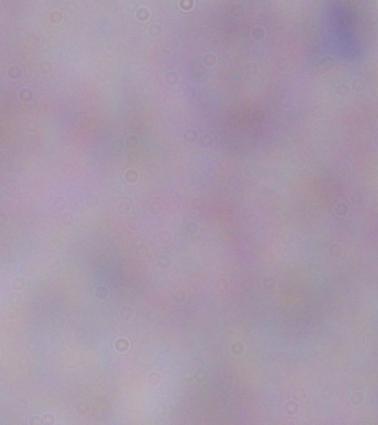
{
  "magnification": "1000x",
  "identification": "trypanosome",
  "modality": "micrograph"
}